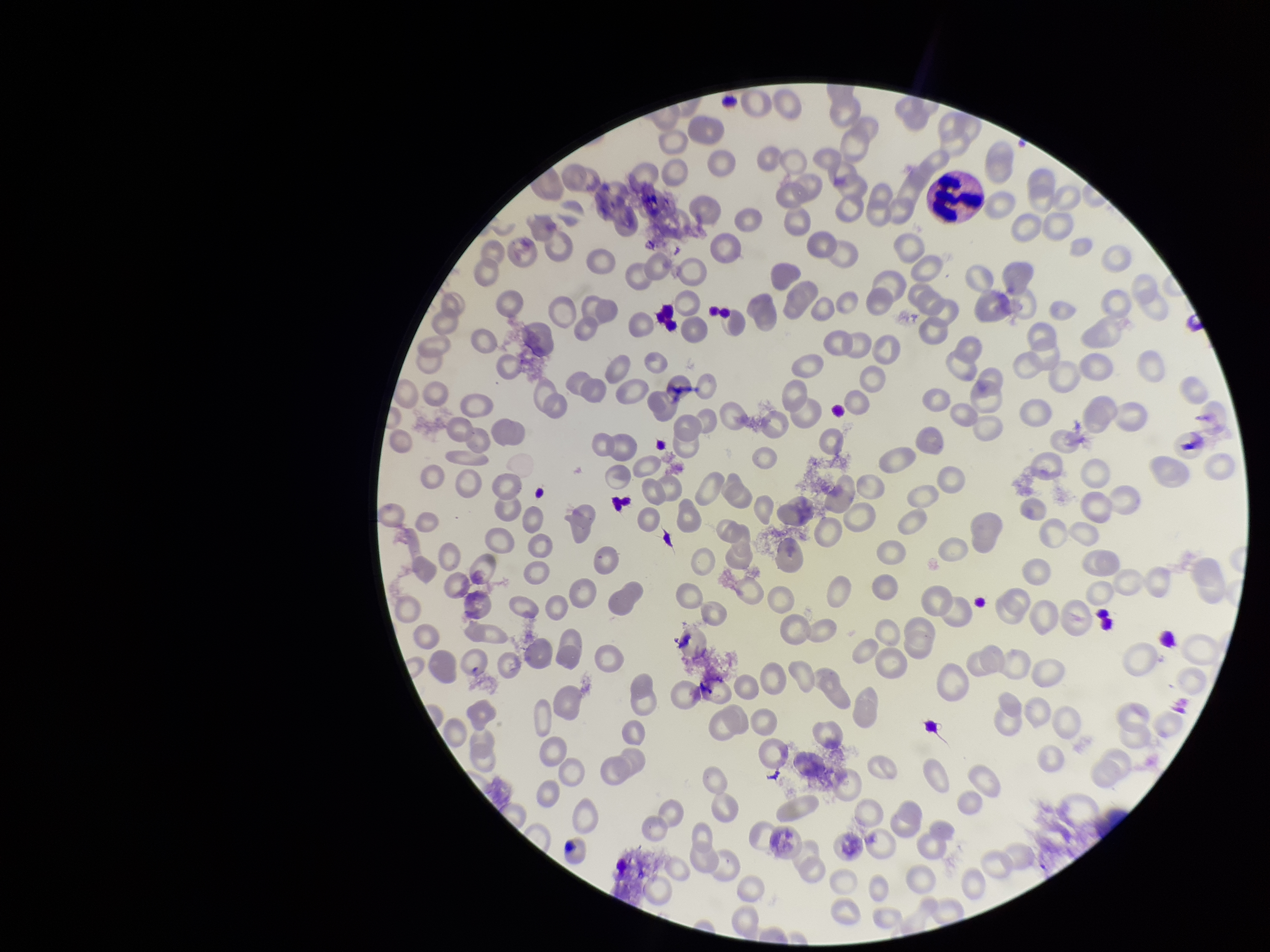

Smartphone photograph taken through the eyepiece of a microscope. Image is 1270×952 pixels. Single field of view. Patient malaria status: negative. Giemsa stain. Parasitized red blood cells: none seen. Parasitized red blood cell count: 0. Red blood cell count: 193. Preparation: thin smear.